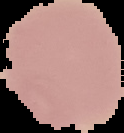

From a thin blood smear. Segmented cell region on a black background. Image is 124×133 pixels. Result: negative for malaria parasites.